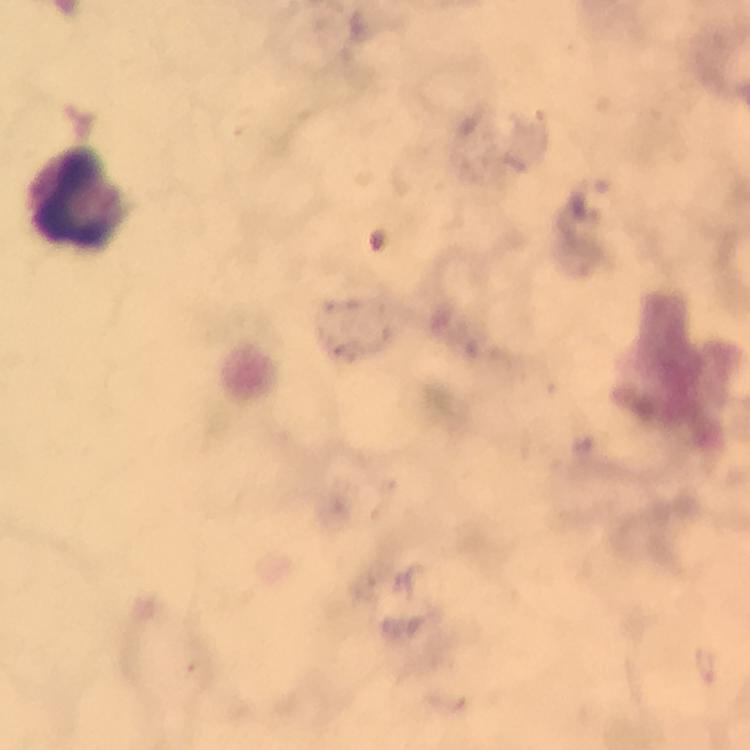
Approximate centers as [x, y] in pixels. Leukocyte locations: [78, 197]. Cropped region of a single field of view. Giemsa stain. 100x magnification. Immersion oil applied. Thick blood smear. Photographed with a smartphone mounted on the microscope. Image is 750×750 pixels. From a malaria diagnostic workup. Malaria parasites: none seen.